Identify the preparation type.
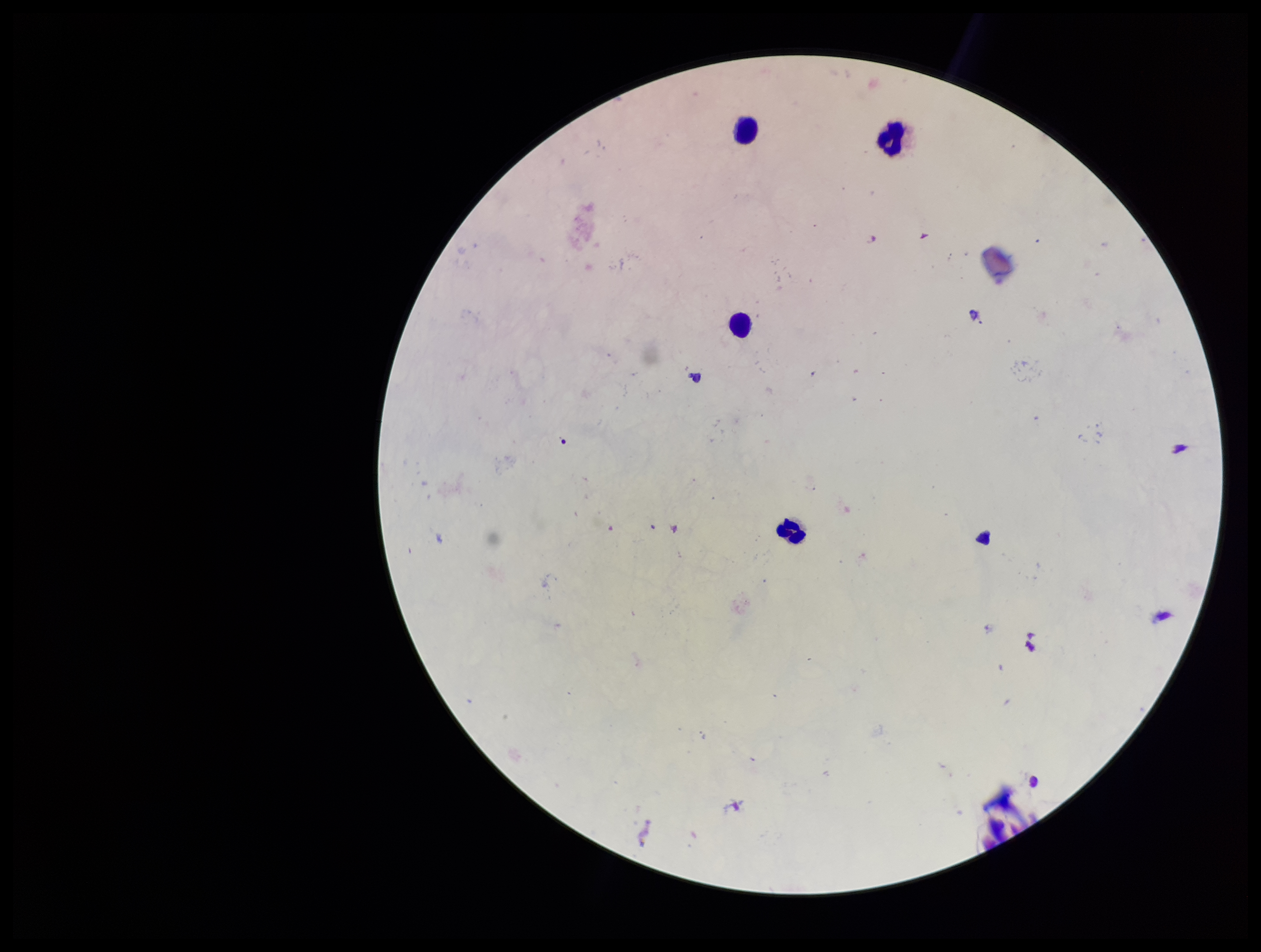

A thick smear.

Parasite count: 0. Plasmodium parasites: none seen. Image is 1261×952 pixels. Photographed through the microscope eyepiece with a smartphone camera. One field from this slide. Stained with Giemsa. Leukocyte count: 4. Patient malaria status: negative.